Classify this cell by malaria status.
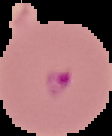

It is parasitized.

The area outside the segmented cell region is set to black. Image is 112×136 pixels. From a thin blood smear.